Identify the parasite.
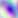

Toxoplasma gondii.

Summary:
  - Magnification: 400x
  - Modality: micrograph